Assess for malaria.
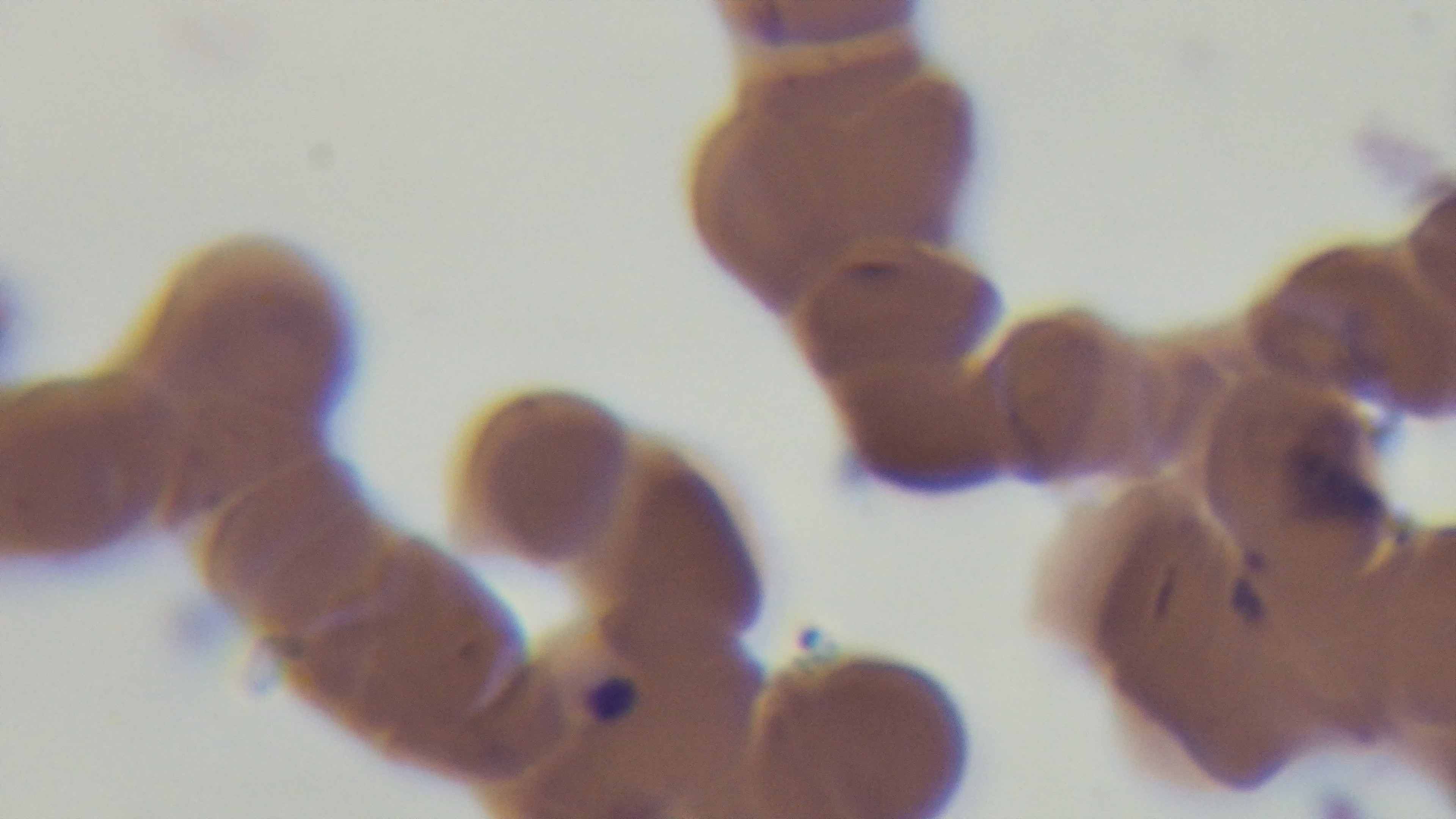
It is infected.

Preparation: thin. Giemsa stain. Mounted 4K digital camera. Single field of view. Oil-immersion objective, 100x. Light microscopy.